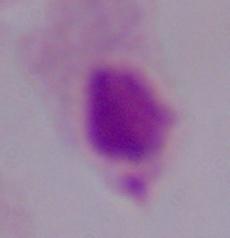

modality = micrograph
magnification = 1000x
identification = trichomonad